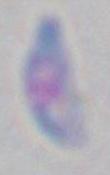
Photomicrograph. Captured at 1000x magnification. Toxoplasma gondii is shown.